Classify this cell by malaria status.
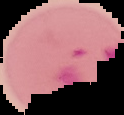
It is parasitized.

Summary:
  - Preparation: thin blood smear
  - Image type: cell region segmented out of the field of view; surrounding area masked to black
  - Image size: 124×115 pixels